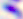

magnification = 400x
modality = photomicrograph
identification = Toxoplasma gondii